Locate every Plasmodium parasite and every leukocyte.
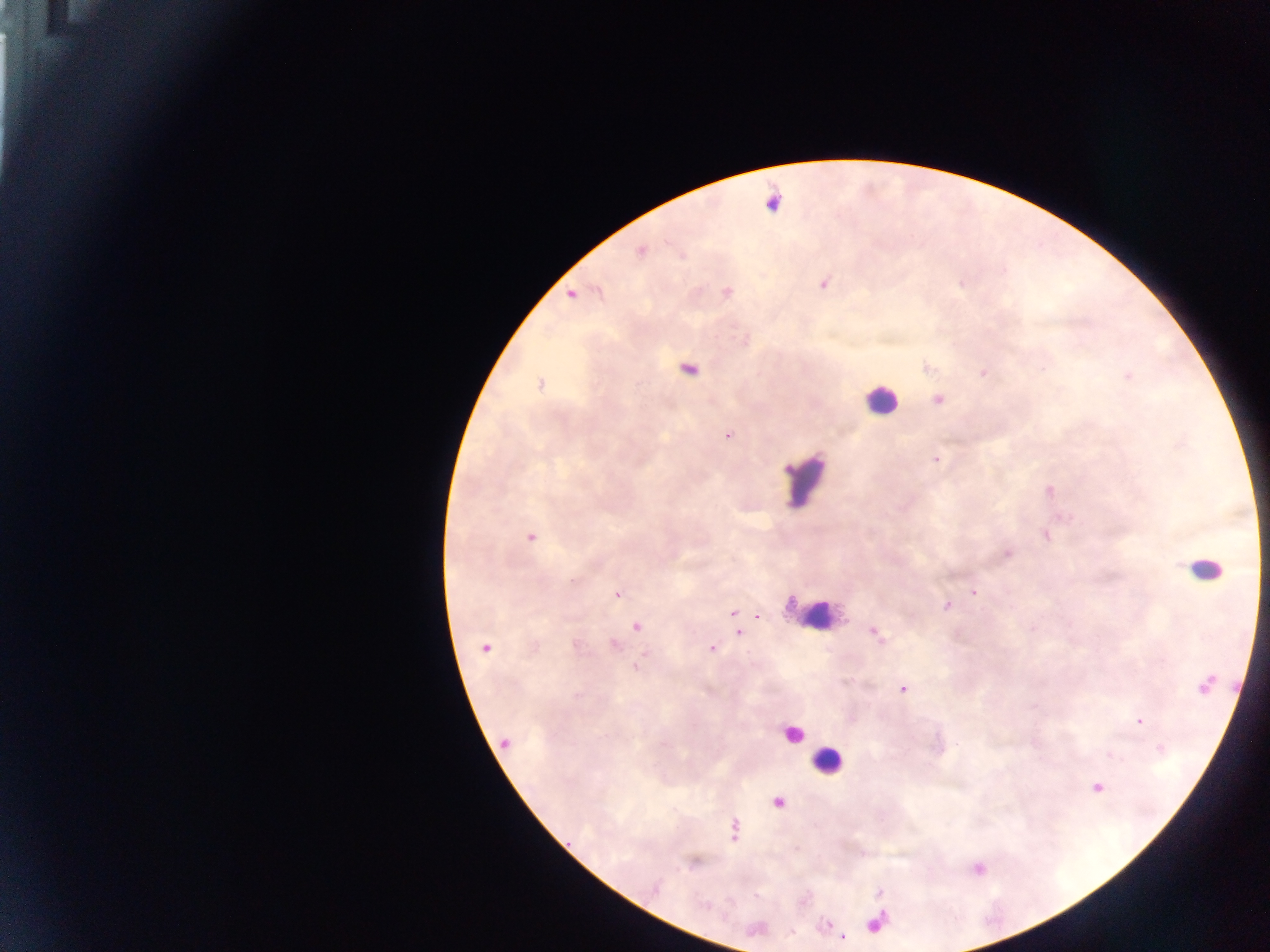
Approximate centers as [x, y] in pixels.
Plasmodium parasites: [772, 203], [639, 250], [822, 282], [597, 290], [726, 291], [571, 294], [687, 368], [926, 368], [983, 373], [1127, 375], [541, 384], [938, 399], [727, 434], [936, 459], [1049, 490], [1045, 534], [530, 536], [1006, 553], [973, 592], [617, 594], [947, 606], [733, 613], [757, 616], [636, 626], [1033, 628], [738, 631], [874, 632], [575, 644], [613, 645], [485, 648], [711, 648], [636, 667], [1204, 685], [902, 688], [1139, 720], [504, 742], [1160, 748], [1097, 786], [777, 802], [733, 829], [826, 924], [842, 937].
Leukocytes: [880, 400], [804, 480], [1206, 569], [814, 614], [791, 734], [827, 760].

{
  "image_size": "1270×952 pixels",
  "field_of_view": "single",
  "preparation": "thick blood smear",
  "capture": "mobile-phone photograph through a microscope",
  "country": "Ghana"
}